Locate and identify every blood parasite.
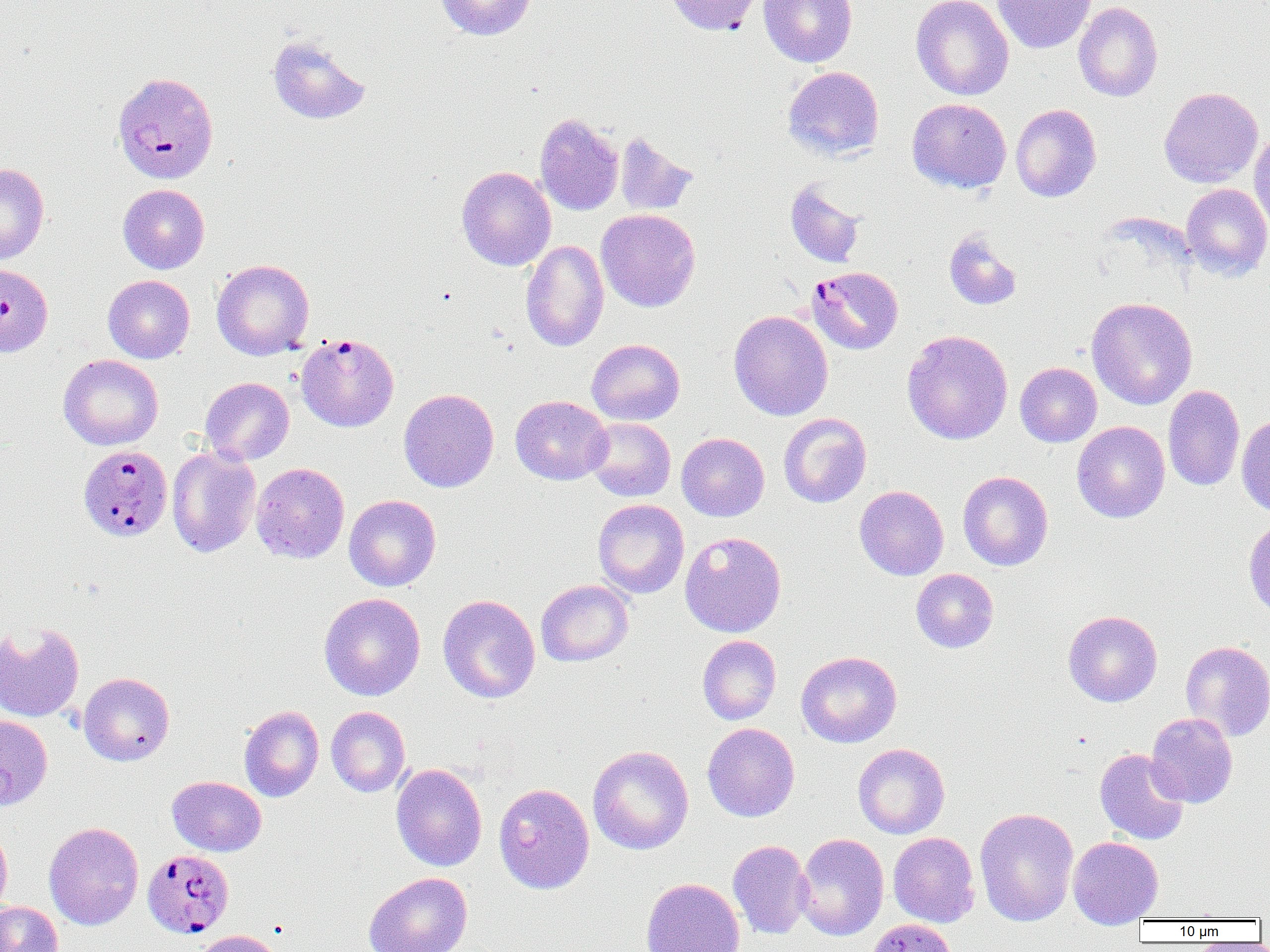
Approximate bounding boxes as (x1,y1)-(x2,y2) corner pairs in pixels.
Plasmodium falciparum-infected red blood cells: (112,72)-(219,184), (0,264)-(53,357), (807,265)-(903,355), (296,332)-(399,431), (78,445)-(173,541), (142,849)-(234,939).
No Plasmodium ovale, Plasmodium malariae, Plasmodium vivax, Babesia divergens, or Trypanosoma brucei observed.

Uninfected red blood cell locations: (436,0)-(536,41), (664,0)-(765,35), (758,0)-(857,67), (911,0)-(1014,100), (992,0)-(1096,54), (1073,1)-(1163,102), (267,34)-(371,125), (782,66)-(884,161), (1159,86)-(1263,187), (907,98)-(1011,193), (1010,103)-(1101,202), (535,112)-(623,215), (1249,129)-(1270,233), (613,132)-(699,217), (0,163)-(49,265), (456,166)-(556,271), (785,180)-(866,268), (1181,183)-(1270,281), (118,184)-(210,274), (596,209)-(700,312), (943,228)-(1022,311), (521,239)-(609,352), (211,258)-(314,360), (103,275)-(195,363), (1087,297)-(1198,410), (728,310)-(833,420), (901,330)-(1013,445), (586,338)-(685,425), (58,354)-(163,450), (1015,362)-(1102,447), (200,377)-(294,465), (1162,385)-(1245,491), (399,388)-(499,492), (511,395)-(612,485), (778,413)-(872,508), (1236,415)-(1270,515), (584,417)-(676,501), (1072,421)-(1170,523), (676,432)-(769,521), (167,446)-(262,558), (251,462)-(349,564), (957,471)-(1053,571), (854,485)-(949,580), (344,494)-(441,591), (592,499)-(690,598), (1243,517)-(1270,620), (679,531)-(786,637), (911,568)-(999,653), (535,579)-(634,667), (319,592)-(425,701), (438,594)-(541,703), (1063,610)-(1162,707), (0,622)-(85,722), (697,635)-(781,724), (1180,640)-(1270,741), (796,650)-(902,747), (78,672)-(175,766), (239,705)-(324,802), (326,706)-(411,797), (1145,713)-(1238,808), (0,714)-(52,810), (702,723)-(800,822), (853,743)-(950,839), (588,745)-(694,855), (1094,748)-(1190,845), (391,763)-(487,871), (167,775)-(266,856), (493,782)-(595,893), (975,807)-(1078,927), (0,821)-(12,917), (43,822)-(144,930), (888,832)-(980,927), (795,833)-(889,941), (1068,836)-(1164,927), (728,840)-(813,939), (363,872)-(473,952), (641,878)-(744,952), (0,901)-(63,952), (865,918)-(958,952), (192,929)-(286,952). Slide-level diagnosis: Plasmodium falciparum. One field of a larger specimen. Image is 1270×952 pixels. Light microscopy. Thin blood film. Captured at 1000x magnification.